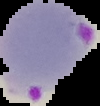 Malaria status: parasitized. Cell region segmented out of the field of view; the surrounding area is masked to black. From a thin blood film. Image is 100×106 pixels.